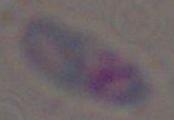
{
  "modality": "photomicrograph",
  "identification": "Toxoplasma gondii",
  "magnification": "1000x"
}